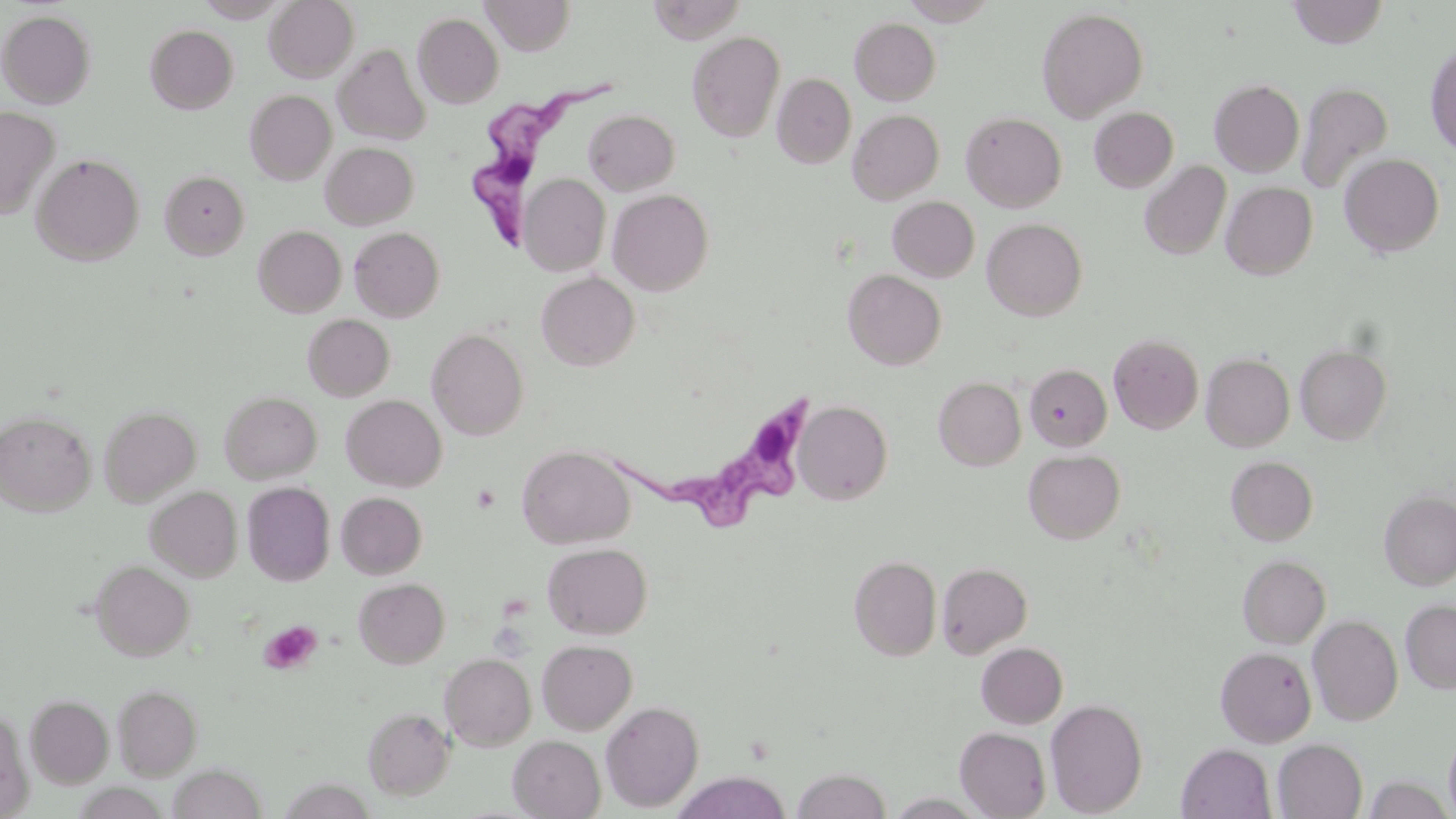

Approximate bounding boxes as [x1, y1, x2, y2] in pixels. Trypanosoma brucei locations: [468, 77, 623, 255], [613, 388, 818, 537]. Uninfected red blood cell locations: [265, 0, 358, 82], [480, 0, 576, 55], [1287, 0, 1388, 48], [647, 1, 747, 44], [1036, 7, 1148, 121], [0, 10, 96, 108], [413, 13, 504, 108], [849, 17, 941, 105], [146, 25, 238, 114], [687, 31, 785, 143], [1425, 40, 1456, 158], [333, 44, 429, 145], [773, 73, 856, 168], [1210, 79, 1304, 177], [1296, 80, 1393, 195], [245, 90, 336, 184], [0, 105, 59, 219], [1089, 107, 1179, 192], [584, 110, 679, 194], [848, 110, 944, 203], [961, 111, 1067, 212], [321, 142, 418, 229], [32, 153, 144, 265], [1339, 153, 1445, 257], [1139, 160, 1232, 260], [160, 170, 250, 259], [520, 174, 610, 275], [1221, 182, 1317, 279], [608, 189, 714, 295], [888, 196, 980, 282], [982, 218, 1087, 320], [254, 225, 346, 317], [349, 227, 445, 321], [843, 269, 946, 369], [536, 271, 639, 370], [303, 314, 395, 401], [427, 328, 528, 440], [1109, 334, 1204, 433], [1295, 344, 1392, 445], [1201, 353, 1294, 451], [1024, 364, 1111, 450], [933, 377, 1026, 470], [219, 391, 322, 483], [341, 395, 446, 491], [795, 400, 892, 504], [99, 405, 201, 506], [0, 410, 96, 515], [518, 445, 635, 548], [1023, 449, 1125, 544], [1226, 456, 1318, 546], [242, 482, 335, 585], [146, 486, 242, 581], [1379, 489, 1456, 590], [336, 492, 427, 579], [542, 542, 652, 638], [1237, 554, 1331, 648], [849, 555, 942, 660], [91, 561, 194, 660], [937, 562, 1032, 658], [354, 578, 450, 668], [1401, 599, 1456, 693], [1308, 614, 1403, 726], [537, 639, 637, 734], [976, 642, 1068, 728], [1216, 647, 1316, 747], [441, 653, 536, 750], [112, 684, 203, 779], [25, 694, 113, 787], [1045, 698, 1148, 817], [601, 701, 704, 811], [362, 706, 455, 800], [0, 707, 32, 816], [1444, 726, 1456, 819], [955, 727, 1051, 818], [508, 735, 605, 818], [1273, 739, 1367, 819], [1177, 744, 1276, 819], [167, 765, 267, 819], [792, 767, 891, 819], [673, 772, 791, 819], [886, 793, 986, 817]. Platelet locations: [470, 483, 501, 513], [259, 620, 321, 675]. Slide-level diagnosis: Trypanosoma brucei. One field of a larger specimen. 1000x magnification. May-Grünwald-Giemsa-stained preparation. Image is 1456×819 pixels. Optical microscopy. Thin blood smear.